Assess this cell for malaria.
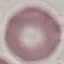
It is uninfected.

Giemsa-stained preparation. Thin blood smear. Acquired by smartphone through the microscope eyepiece. Cell patch, automatically extracted from a larger field of view and resized to 64 × 64 pixels.